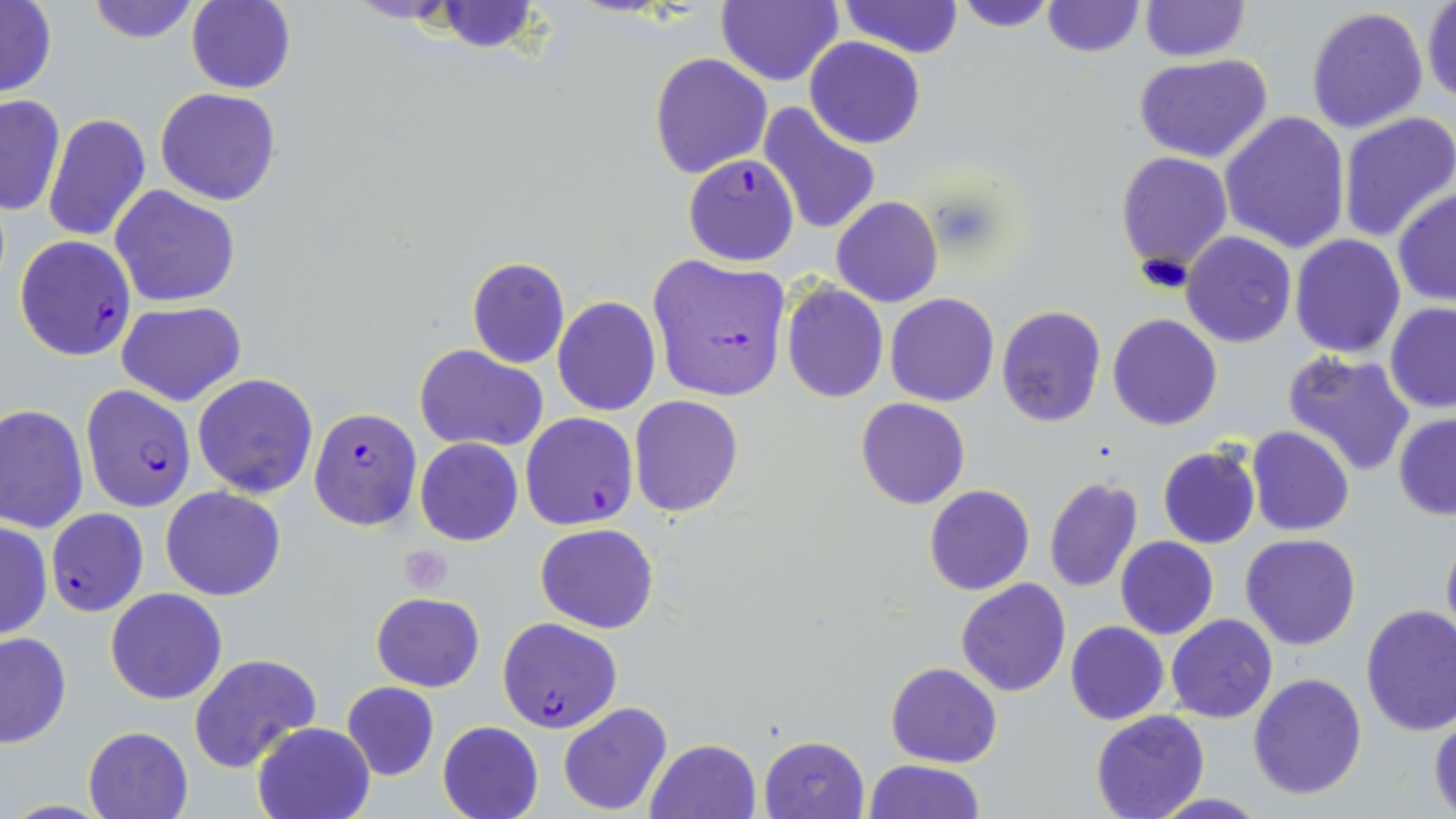
Approximate bounding boxes as (x1,y1)-(x2,y2) corner pairs in pixels. Uninfected red blood cell locations: (84,0)-(200,45), (837,0)-(965,58), (953,0)-(1058,32), (0,1)-(57,99), (186,1)-(295,93), (432,1)-(541,53), (715,1)-(843,86), (1041,1)-(1143,57), (1139,1)-(1250,63), (1422,1)-(1456,106), (1306,6)-(1430,135), (806,37)-(926,148), (649,54)-(772,178), (1133,55)-(1275,164), (156,88)-(280,207), (0,93)-(66,216), (758,101)-(881,237), (1219,110)-(1350,253), (42,112)-(150,243), (1336,112)-(1456,243), (1115,151)-(1233,277), (109,185)-(241,309), (1391,188)-(1455,306), (832,196)-(942,307), (1182,231)-(1297,348), (1290,233)-(1406,357), (466,256)-(569,368), (781,283)-(887,402), (886,294)-(999,407), (553,297)-(660,417), (115,300)-(247,406), (881,301)-(1103,418), (1384,303)-(1456,413), (995,305)-(1106,429), (1107,312)-(1224,431), (414,344)-(548,453), (1282,350)-(1416,478), (192,372)-(319,497), (629,396)-(742,517), (856,397)-(969,510), (0,405)-(88,535), (1393,412)-(1456,522), (1246,427)-(1353,536), (415,439)-(523,546), (1157,445)-(1261,549), (1043,475)-(1144,592), (924,485)-(1034,595), (161,486)-(286,601), (0,520)-(51,642), (536,522)-(658,634), (1440,526)-(1456,654), (1241,534)-(1362,651), (1116,536)-(1219,639), (956,578)-(1071,696), (105,588)-(228,706), (371,592)-(486,692), (1359,606)-(1456,737), (1165,613)-(1278,722), (1065,620)-(1169,724), (0,632)-(72,749), (189,652)-(322,775), (884,662)-(1002,767), (1247,672)-(1366,800), (340,682)-(439,781), (557,703)-(673,816), (1090,711)-(1211,819), (1429,718)-(1456,815), (437,720)-(545,819), (251,721)-(375,819), (82,725)-(194,819), (759,735)-(869,818), (643,738)-(763,819), (863,759)-(984,818), (1150,793)-(1271,819). Plasmodium falciparum-infected red blood cell locations: (683,154)-(799,266), (14,236)-(136,361), (646,255)-(791,404), (79,390)-(197,512), (309,407)-(422,531), (520,412)-(638,530), (46,508)-(147,616), (497,617)-(622,734). Platelet locations: (400,546)-(453,594). Slide-level diagnosis: Plasmodium falciparum. Thin blood smear. Image is 1456×819 pixels. Optical microscopy. Captured at 1000x magnification. One field of a larger specimen. May-Grünwald-Giemsa stain.